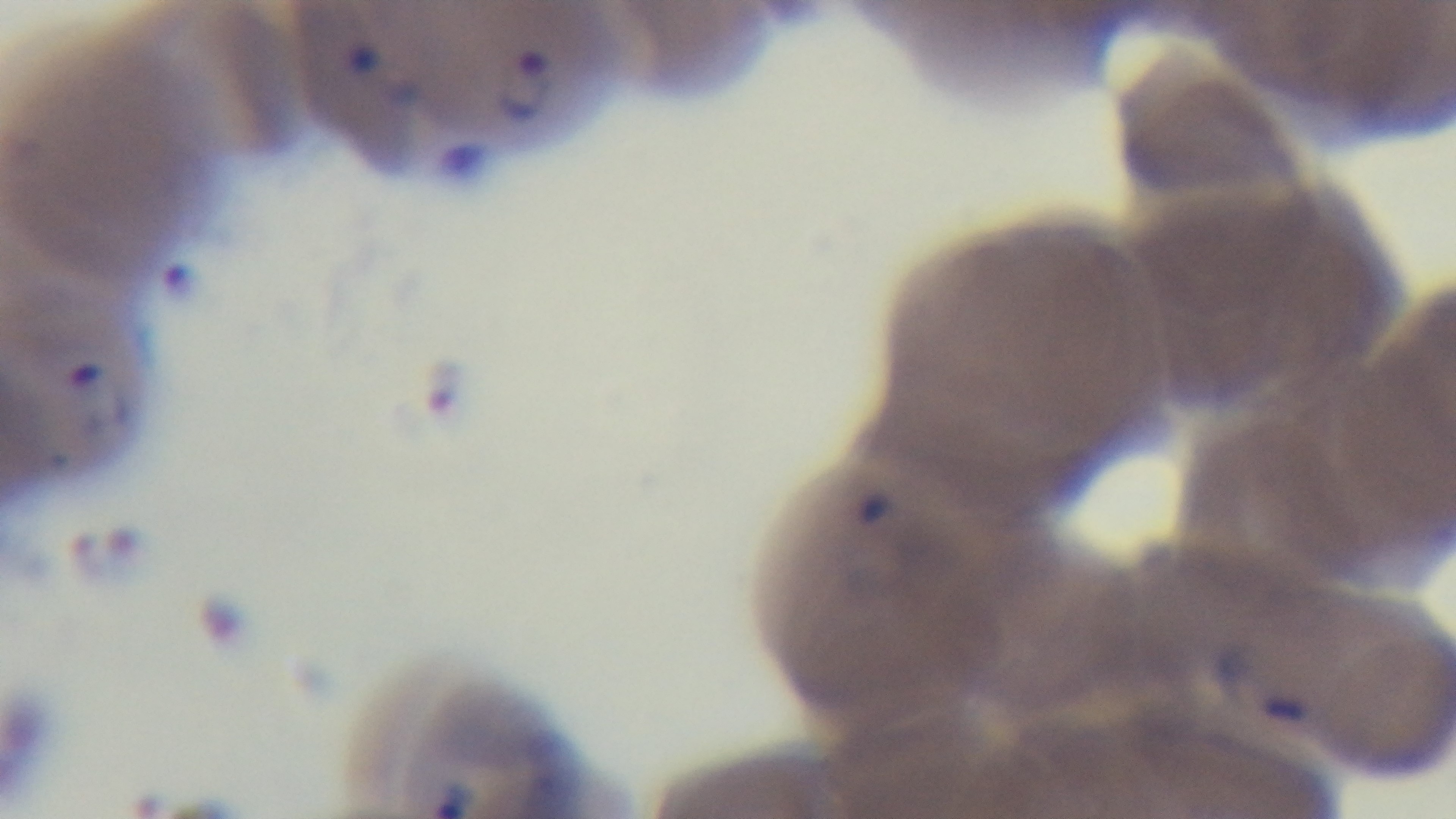 100x oil-immersion objective. Single field of view. Malaria status: positive. Mounted 4K digital camera. Giemsa-stained. Light microscopy. Preparation: thin smear.